Name the blood parasite species.
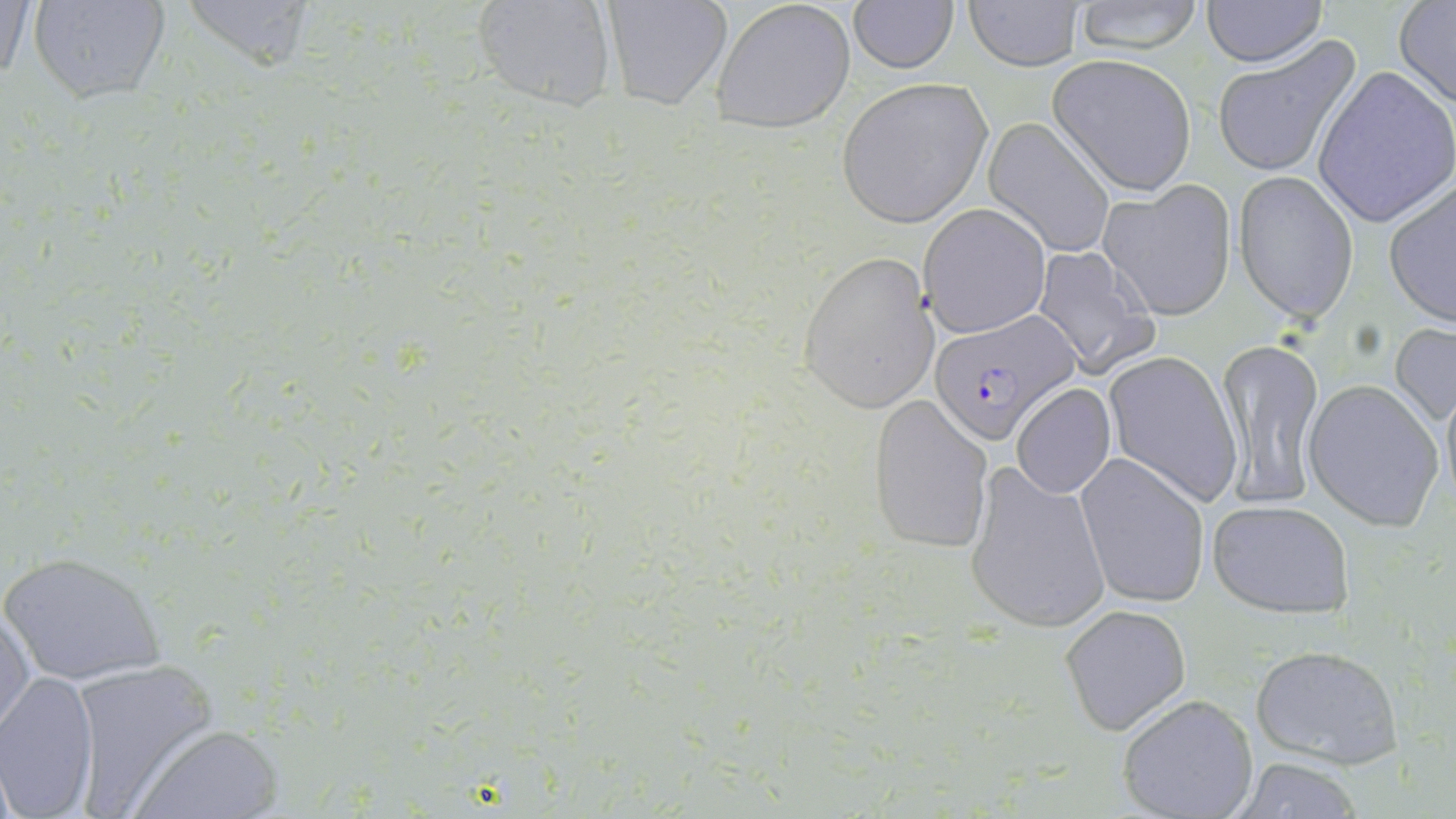

Plasmodium falciparum.

Approximate bounding boxes as (x1,y1)-(x2,y2) corner pairs in pixels. Uninfected red blood cell locations: (1,0)-(35,93), (26,0)-(170,104), (173,0)-(320,74), (471,0)-(621,113), (597,0)-(732,112), (710,0)-(856,133), (1068,0)-(1209,53), (1200,0)-(1328,67), (963,1)-(1085,71), (1394,1)-(1456,108), (845,2)-(960,75), (1211,37)-(1362,178), (1048,55)-(1197,195), (1313,67)-(1456,228), (835,76)-(993,229), (984,118)-(1115,256), (1234,173)-(1358,324), (1384,178)-(1456,329), (1100,180)-(1237,321), (920,204)-(1050,338), (1031,244)-(1160,378), (798,249)-(938,412), (1389,321)-(1456,424), (1214,336)-(1327,509), (1103,350)-(1242,508), (1439,374)-(1456,513), (1304,381)-(1444,532), (1012,383)-(1116,499), (870,395)-(995,553), (1075,452)-(1213,609), (964,459)-(1111,634), (1206,497)-(1356,619), (2,550)-(164,688), (0,601)-(34,738), (1060,604)-(1191,737), (1246,642)-(1405,770), (67,660)-(219,811), (0,672)-(100,818), (1118,693)-(1260,818), (130,723)-(283,817), (1230,759)-(1368,817). Plasmodium falciparum-infected red blood cell locations: (927,314)-(1079,445). Image is 1456×819 pixels. One field of a larger specimen. Thin blood smear. May-Grünwald-Giemsa-stained preparation. Optical microscopy. Captured at 1000x magnification.